Identify the preparation type.
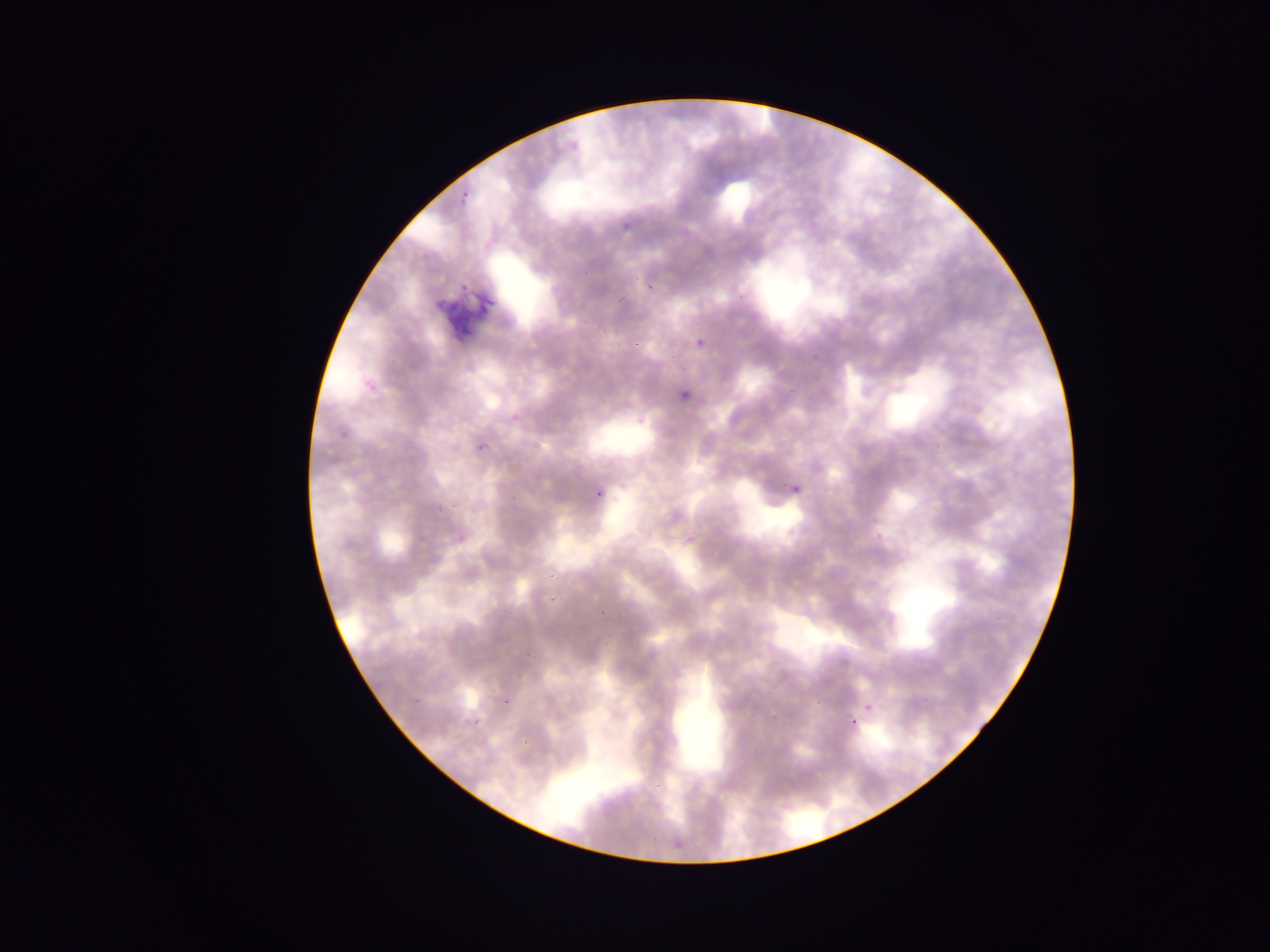

This is a thin smear.

Approximate bounding boxes as [left, top, right, bottom] in pixels. Plasmodium parasite locations: [463, 189, 470, 197], [459, 198, 465, 206], [619, 222, 637, 232], [646, 282, 653, 290], [690, 336, 703, 351], [630, 344, 641, 347], [364, 377, 374, 383], [683, 390, 690, 400], [510, 412, 521, 424], [342, 427, 349, 438], [476, 441, 489, 454], [793, 481, 801, 497], [593, 488, 609, 503], [454, 531, 469, 545], [599, 608, 605, 616], [504, 689, 519, 708], [413, 695, 422, 705], [865, 699, 877, 712], [844, 715, 858, 724], [473, 719, 480, 727], [670, 831, 685, 852] | approximate [x, y] pixel centers of objects too small to bound: [585, 273], [372, 388], [552, 575], [552, 599]. Artifact (stain precipitate or debris) locations: [434, 268, 505, 347]. Collected in Ghana. Mobile-phone photograph taken through the microscope. Image is 1270×952 pixels. Single field of view.